Outline each uninfected red blood cell.
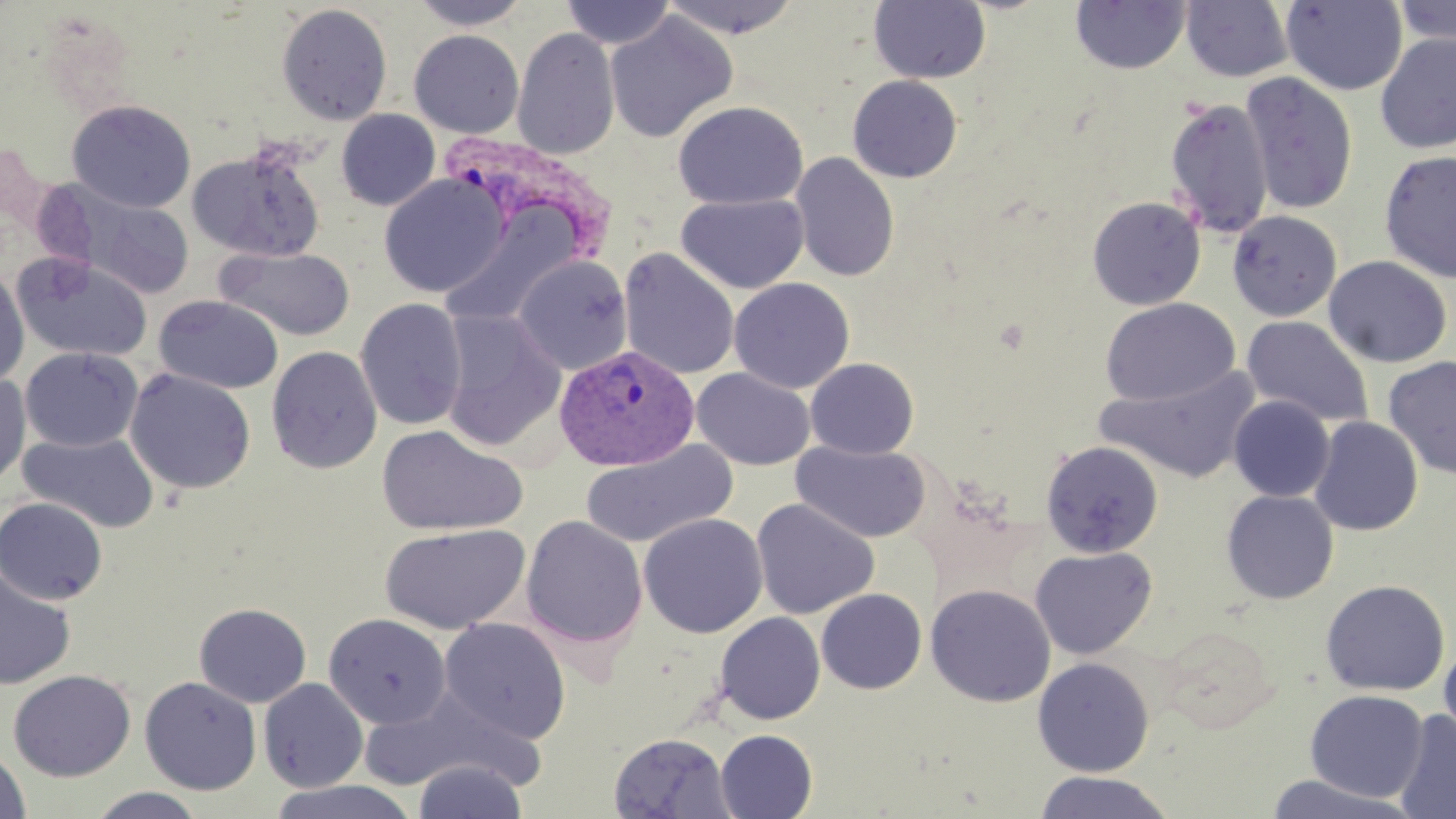
Approximate bounding boxes as [x1, y1, x2, y2] in pixels.
Uninfected red blood cells: [409, 0, 532, 30], [560, 0, 675, 49], [659, 0, 803, 40], [868, 0, 991, 84], [1392, 0, 1456, 48], [1070, 1, 1192, 74], [1180, 1, 1294, 82], [1281, 1, 1407, 95], [276, 3, 393, 126], [604, 12, 738, 143], [512, 27, 620, 160], [408, 30, 524, 138], [1374, 32, 1456, 154], [1240, 71, 1358, 214], [847, 75, 963, 183], [1165, 98, 1274, 238], [67, 99, 196, 213], [673, 100, 808, 210], [337, 108, 441, 210], [187, 143, 326, 261], [1378, 149, 1456, 283], [790, 151, 900, 282], [378, 173, 510, 298], [50, 183, 197, 301], [676, 193, 810, 294], [1086, 196, 1206, 310], [438, 207, 587, 330], [1227, 210, 1343, 322], [216, 246, 356, 341], [618, 248, 740, 380], [11, 253, 154, 361], [513, 255, 632, 375], [1323, 255, 1453, 368], [0, 267, 29, 388], [729, 277, 854, 394], [153, 294, 284, 394], [354, 298, 468, 431], [1100, 298, 1240, 407], [440, 310, 567, 452], [1241, 315, 1373, 428], [266, 345, 382, 474], [19, 347, 142, 452], [1382, 355, 1456, 479], [805, 358, 919, 460], [1096, 365, 1264, 483], [124, 367, 256, 494], [691, 367, 815, 470], [0, 373, 31, 489], [1228, 395, 1335, 502], [1308, 415, 1424, 536], [376, 424, 528, 537], [18, 430, 159, 533], [578, 439, 739, 549], [1039, 440, 1163, 558], [793, 441, 932, 543], [1221, 490, 1339, 605], [0, 497, 108, 605], [751, 497, 879, 619], [638, 513, 768, 638], [520, 515, 648, 650], [379, 523, 530, 635], [1030, 546, 1157, 660], [0, 570, 76, 690], [1320, 579, 1450, 696], [925, 584, 1056, 707], [816, 588, 927, 694], [194, 602, 311, 708], [715, 611, 826, 724], [323, 612, 451, 730], [438, 617, 571, 745], [1439, 639, 1456, 750], [1032, 657, 1155, 777], [8, 669, 136, 781], [139, 676, 262, 795], [258, 678, 368, 792], [361, 689, 538, 794], [1304, 689, 1429, 803], [1393, 709, 1456, 819], [715, 729, 817, 818], [608, 732, 735, 818], [0, 747, 31, 819], [412, 759, 528, 819], [1033, 770, 1177, 819], [1261, 774, 1422, 818], [261, 779, 425, 819], [86, 788, 207, 818].

slide_level_diagnosis: Plasmodium vivax
preparation: thin blood film
magnification: 1000x
stain: May-Grünwald-Giemsa
image_size: 1456×819 pixels
plasmodium_vivax_infected_red_blood_cell_locations: 'approximate bounding boxes as [x1, y1, x2, y2] in pixels: [440, 131, 621, 258], [554, 344, 699, 471]'
field_of_view: one of a larger specimen
modality: optical microscopy